Classify this cell by malaria status.
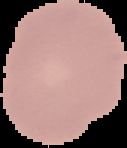
It is uninfected.

Summary:
  - Image type: segmented cell region on a black background
  - Image size: 127×148 pixels
  - Preparation: thin blood film